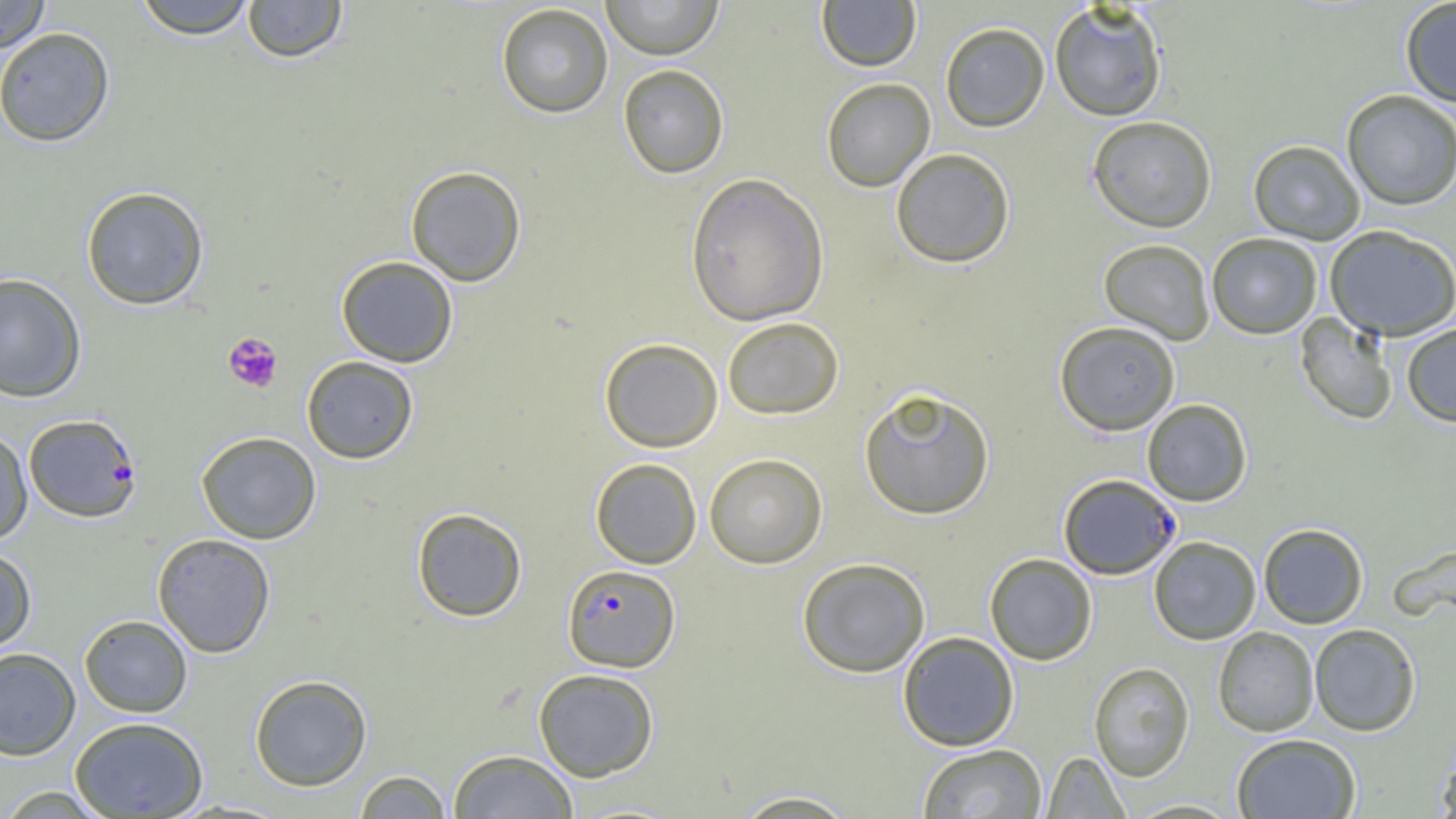
slide-level diagnosis = Plasmodium falciparum
platelet locations = approximate bounding boxes as named x1/y1/x2/y2 corners in pixels: (x1=223, y1=333, x2=283, y2=393)
preparation = thin blood film
Plasmodium falciparum-infected red blood cell locations = approximate bounding boxes as named x1/y1/x2/y2 corners in pixels: (x1=23, y1=413, x2=142, y2=523), (x1=1058, y1=473, x2=1181, y2=580), (x1=562, y1=564, x2=680, y2=672)
image size = 1456×819 pixels
field of view = single
uninfected red blood cell locations = approximate bounding boxes as named x1/y1/x2/y2 corners in pixels: (x1=0, y1=0, x2=52, y2=54), (x1=132, y1=0, x2=258, y2=39), (x1=242, y1=0, x2=348, y2=63), (x1=600, y1=0, x2=724, y2=59), (x1=1399, y1=0, x2=1456, y2=108), (x1=815, y1=1, x2=921, y2=72), (x1=496, y1=3, x2=613, y2=118), (x1=1049, y1=3, x2=1168, y2=122), (x1=939, y1=21, x2=1050, y2=132), (x1=0, y1=27, x2=116, y2=147), (x1=617, y1=64, x2=729, y2=179), (x1=821, y1=77, x2=936, y2=192), (x1=1341, y1=90, x2=1456, y2=211), (x1=1087, y1=115, x2=1218, y2=232), (x1=1248, y1=139, x2=1366, y2=245), (x1=890, y1=148, x2=1015, y2=269), (x1=405, y1=165, x2=527, y2=286), (x1=685, y1=172, x2=830, y2=326), (x1=81, y1=185, x2=210, y2=310), (x1=1325, y1=224, x2=1456, y2=341), (x1=1206, y1=233, x2=1323, y2=339), (x1=1098, y1=238, x2=1215, y2=345), (x1=336, y1=256, x2=459, y2=367), (x1=0, y1=272, x2=87, y2=402), (x1=1294, y1=312, x2=1399, y2=426), (x1=721, y1=317, x2=845, y2=420), (x1=1054, y1=321, x2=1181, y2=435), (x1=1401, y1=322, x2=1456, y2=427), (x1=598, y1=337, x2=723, y2=452), (x1=301, y1=355, x2=419, y2=464), (x1=858, y1=387, x2=996, y2=520), (x1=1141, y1=399, x2=1253, y2=506), (x1=0, y1=427, x2=33, y2=545), (x1=196, y1=431, x2=322, y2=544), (x1=703, y1=453, x2=828, y2=568), (x1=590, y1=457, x2=702, y2=569), (x1=411, y1=507, x2=527, y2=622), (x1=1257, y1=523, x2=1369, y2=629), (x1=152, y1=533, x2=276, y2=657), (x1=1149, y1=536, x2=1261, y2=645), (x1=1390, y1=542, x2=1456, y2=628), (x1=0, y1=546, x2=36, y2=655), (x1=984, y1=553, x2=1098, y2=665), (x1=796, y1=556, x2=931, y2=678), (x1=79, y1=614, x2=193, y2=717), (x1=1309, y1=623, x2=1421, y2=736), (x1=1213, y1=626, x2=1319, y2=737), (x1=897, y1=631, x2=1019, y2=751), (x1=0, y1=647, x2=81, y2=760), (x1=1088, y1=662, x2=1195, y2=781), (x1=533, y1=668, x2=659, y2=782), (x1=249, y1=674, x2=372, y2=791), (x1=70, y1=716, x2=209, y2=818), (x1=1231, y1=733, x2=1362, y2=819), (x1=1435, y1=739, x2=1456, y2=819), (x1=916, y1=743, x2=1048, y2=818), (x1=447, y1=749, x2=578, y2=818), (x1=1041, y1=751, x2=1130, y2=818), (x1=353, y1=770, x2=452, y2=818), (x1=0, y1=785, x2=113, y2=819), (x1=729, y1=789, x2=862, y2=818)
magnification = 1000x
modality = optical microscopy